Identify the parasite.
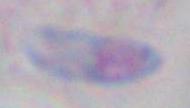

Toxoplasma gondii.

Summary:
  - Modality: micrograph
  - Magnification: 1000x